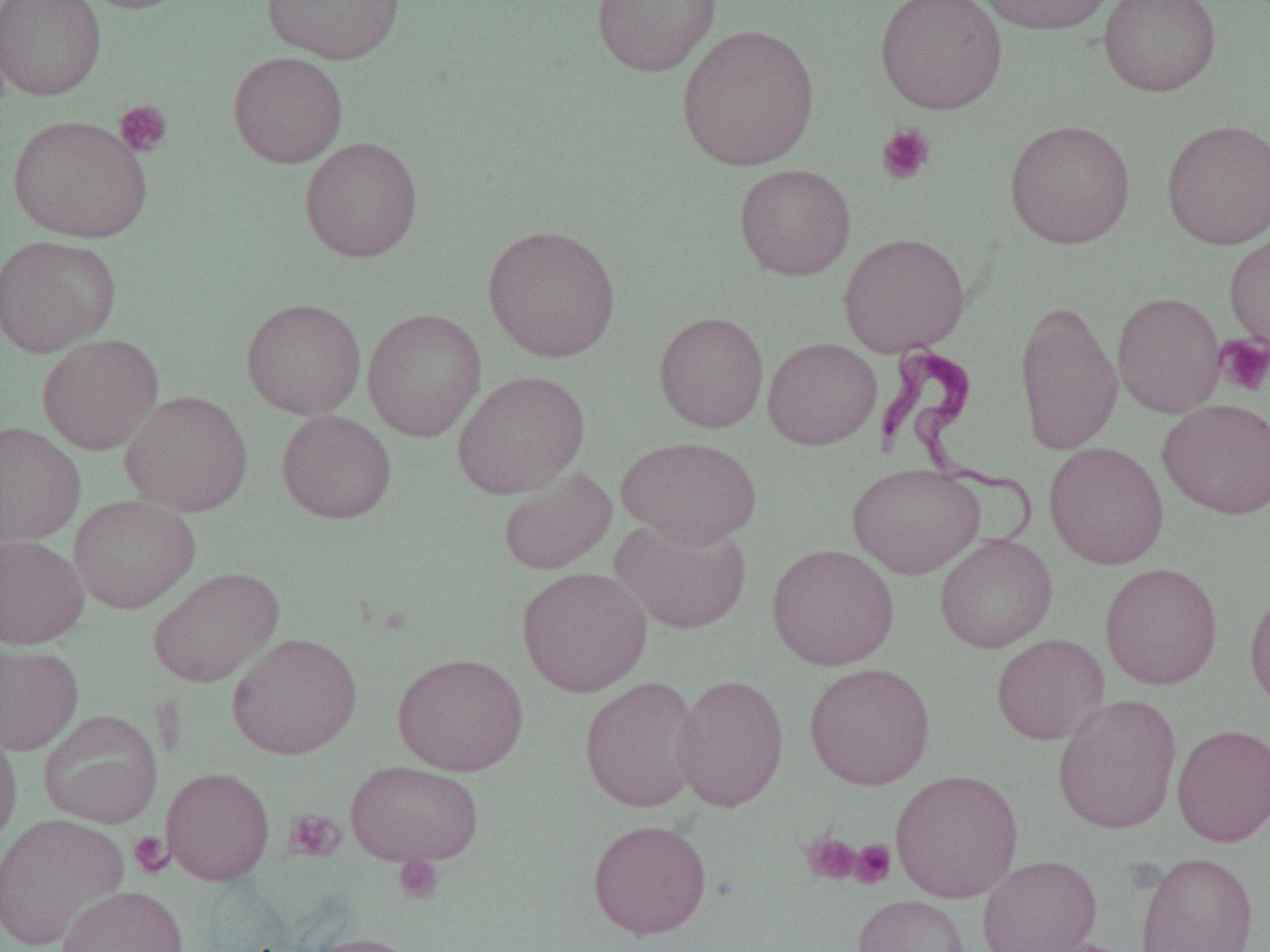
Approximate bounding boxes as (x1, y1, x2, y2) in pixels. Trypanosoma brucei locations: (876, 341, 1039, 548). Uninfected red blood cell locations (subset): (0, 0, 106, 101), (77, 0, 194, 14), (262, 0, 405, 64), (591, 0, 720, 77), (971, 0, 1119, 35), (1098, 0, 1221, 97), (676, 23, 821, 172), (228, 51, 349, 168), (8, 114, 153, 243), (1004, 119, 1136, 249), (1161, 119, 1270, 250), (299, 136, 423, 262), (734, 164, 856, 280), (482, 224, 621, 362), (1224, 230, 1270, 354), (838, 232, 971, 357), (0, 235, 120, 357), (1112, 291, 1226, 418), (242, 298, 366, 419), (1014, 299, 1124, 454), (362, 307, 487, 443), (654, 311, 769, 433), (37, 334, 164, 455), (762, 337, 882, 450), (452, 370, 590, 499), (120, 390, 253, 517), (1157, 398, 1270, 519), (276, 410, 397, 524), (0, 422, 86, 546), (615, 436, 762, 549), (1044, 441, 1169, 570), (847, 463, 985, 579), (498, 467, 618, 575), (68, 494, 200, 613), (610, 516, 751, 634), (935, 534, 1058, 653), (0, 535, 89, 649), (767, 543, 899, 671), (1100, 562, 1223, 690), (148, 567, 284, 688), (516, 567, 652, 697), (1244, 586, 1270, 711), (227, 632, 362, 760), (991, 633, 1109, 745), (0, 643, 84, 756), (392, 652, 529, 776), (804, 662, 936, 790), (671, 673, 789, 812), (579, 675, 704, 814), (1053, 693, 1182, 834), (38, 709, 163, 829), (1171, 723, 1270, 847), (0, 725, 22, 851), (345, 760, 485, 867), (161, 767, 274, 885), (889, 769, 1023, 904), (0, 813, 129, 951), (588, 818, 711, 940), (1134, 850, 1259, 952), (977, 854, 1102, 952), (56, 885, 189, 952), (852, 894, 970, 952), (305, 931, 428, 952). Platelet locations (subset): (115, 99, 172, 157), (876, 123, 936, 185), (1214, 333, 1270, 396), (284, 809, 345, 862), (801, 830, 862, 885), (128, 831, 172, 878), (850, 839, 896, 889), (394, 855, 444, 904). Slide-level diagnosis: Trypanosoma brucei. 1000x magnification. Thin blood smear. Optical microscopy. One field of a larger specimen. Image is 1270×952 pixels.